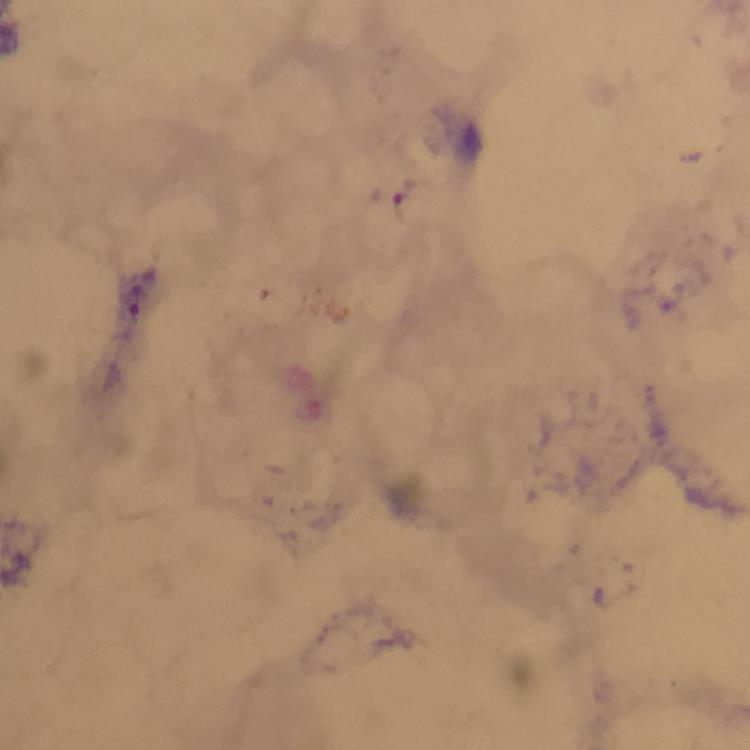
Approximate centers as (x, y) in pixels.
Summary:
  - Malaria parasite locations: (403, 194), (136, 301)
  - Stain: Giemsa
  - Image size: 750×750 pixels
  - Immersion oil: applied
  - Cropped from: one field of view
  - Magnification: 100x
  - Context: from a diagnostic examination for malaria
  - Capture: smartphone photograph through a microscope
  - Preparation: thick blood film